Outline each blood parasite and name the species.
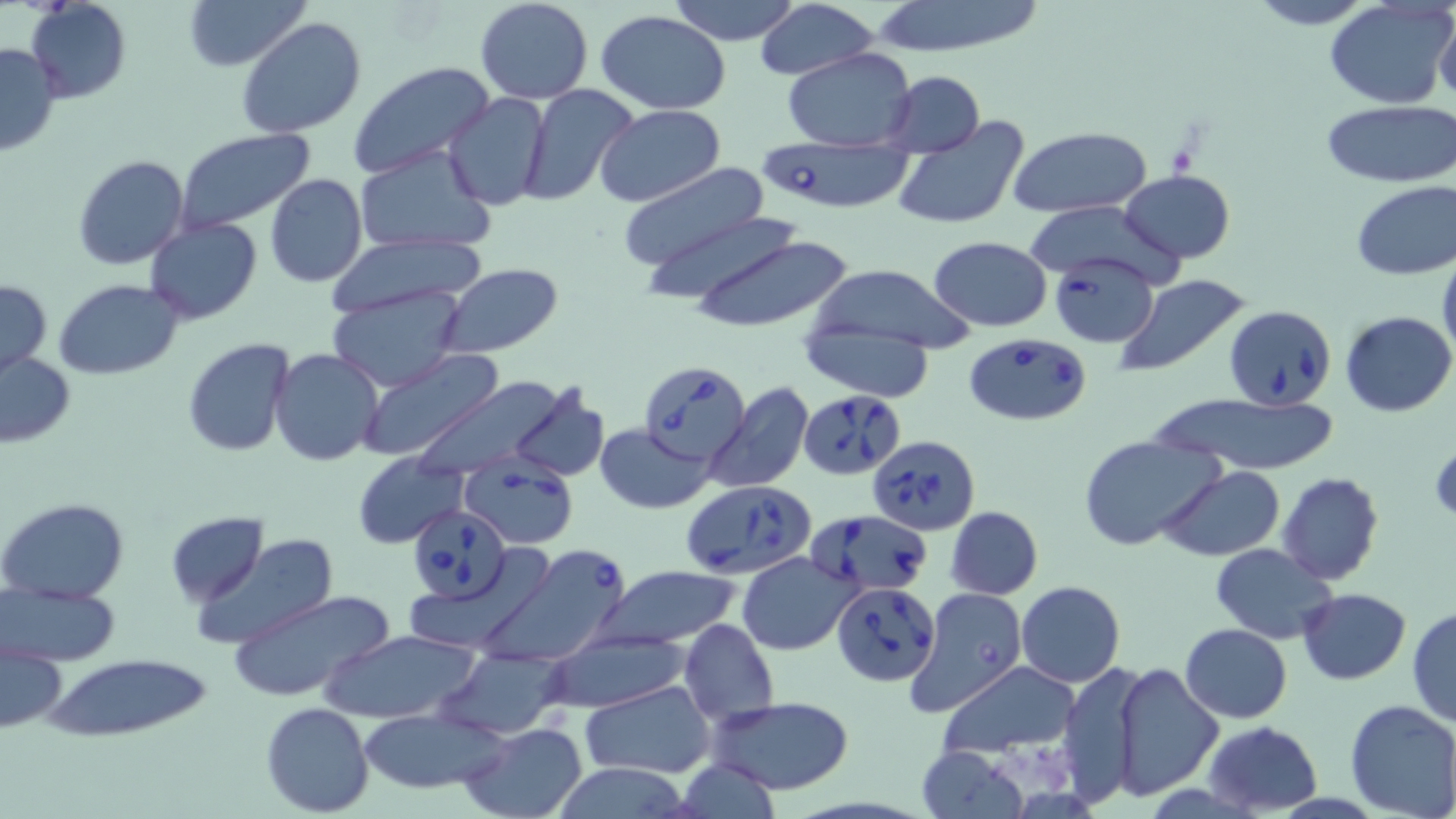

Approximate bounding boxes as (x1, y1, x2, y2) in pixels.
Babesia divergens-infected red blood cells: (753, 138, 919, 215), (1049, 253, 1160, 347), (1225, 304, 1339, 410), (961, 333, 1093, 427), (640, 362, 750, 464), (799, 385, 911, 480), (867, 434, 980, 535), (460, 458, 577, 549), (681, 482, 817, 579), (409, 505, 513, 603), (805, 509, 932, 593), (477, 543, 631, 669), (832, 581, 940, 686).
No Plasmodium falciparum, Plasmodium ovale, Plasmodium malariae, Plasmodium vivax, or Trypanosoma brucei observed.

Summary:
  - Uninfected red blood cell locations: (180, 0, 309, 74), (474, 0, 594, 104), (664, 0, 806, 46), (863, 0, 1049, 58), (1244, 0, 1377, 28), (26, 1, 132, 102), (1323, 1, 1453, 111), (754, 4, 883, 81), (1433, 8, 1456, 106), (595, 10, 733, 112), (236, 17, 368, 138), (0, 41, 63, 159), (781, 48, 919, 150), (347, 61, 496, 179), (880, 73, 986, 156), (518, 85, 641, 206), (443, 93, 551, 211), (1321, 101, 1455, 188), (594, 104, 725, 207), (893, 116, 1032, 234), (1008, 125, 1151, 216), (174, 127, 316, 234), (354, 145, 496, 260), (72, 154, 189, 271), (620, 163, 776, 282), (1121, 169, 1235, 263), (264, 174, 367, 290), (1350, 181, 1456, 279), (635, 208, 798, 302), (145, 218, 263, 324), (679, 225, 856, 334), (324, 233, 490, 314), (927, 236, 1053, 331), (1437, 250, 1456, 366), (436, 263, 563, 357), (800, 263, 978, 356), (1113, 273, 1255, 381), (0, 278, 51, 377), (54, 279, 185, 379), (326, 287, 468, 391), (1341, 310, 1456, 417), (797, 328, 938, 401), (182, 338, 296, 457), (268, 348, 385, 467), (358, 349, 504, 463), (1, 351, 76, 448), (402, 376, 578, 479), (705, 382, 812, 493), (504, 384, 611, 485), (1157, 394, 1341, 474), (597, 423, 714, 514), (1079, 436, 1222, 551), (353, 454, 468, 548), (1158, 465, 1286, 561), (1276, 472, 1385, 586), (0, 497, 130, 602), (944, 506, 1042, 599), (166, 512, 265, 607), (190, 534, 338, 649), (1210, 544, 1337, 643), (737, 551, 857, 656), (407, 556, 548, 651), (599, 565, 742, 648), (1016, 581, 1125, 686), (4, 585, 119, 666), (906, 587, 1026, 715), (1298, 587, 1412, 685), (228, 588, 396, 703), (1407, 606, 1455, 727), (680, 620, 779, 728), (1180, 623, 1291, 722), (319, 628, 481, 725), (540, 629, 691, 713), (1, 640, 67, 734), (434, 650, 566, 739), (45, 656, 214, 742), (938, 660, 1080, 756), (1057, 660, 1150, 806), (1112, 663, 1225, 799), (580, 681, 714, 780), (707, 697, 857, 795), (1344, 698, 1456, 819), (261, 702, 375, 817), (354, 707, 508, 796), (458, 721, 589, 819), (1203, 721, 1321, 814), (915, 744, 1028, 819), (674, 756, 782, 819), (549, 763, 699, 819)
  - Slide-level diagnosis: Babesia divergens
  - Modality: light microscopy
  - Stain: May-Grünwald-Giemsa
  - Field of view: single
  - Magnification: 1000x
  - Image size: 1456×819 pixels
  - Preparation: thin blood film